State which parasite is depicted.
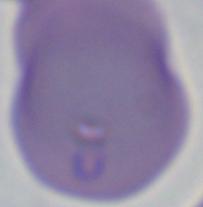
This is Babesia.

modality = photomicrograph
magnification = 1000x